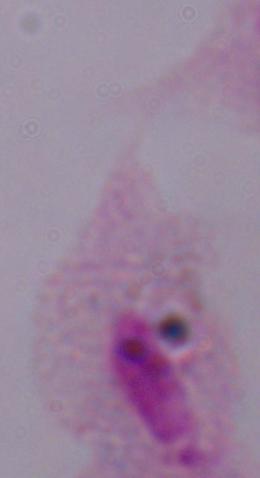 Captured at 1000x magnification. A trichomonad is seen. Micrograph.